Evaluate for Plasmodium parasites.
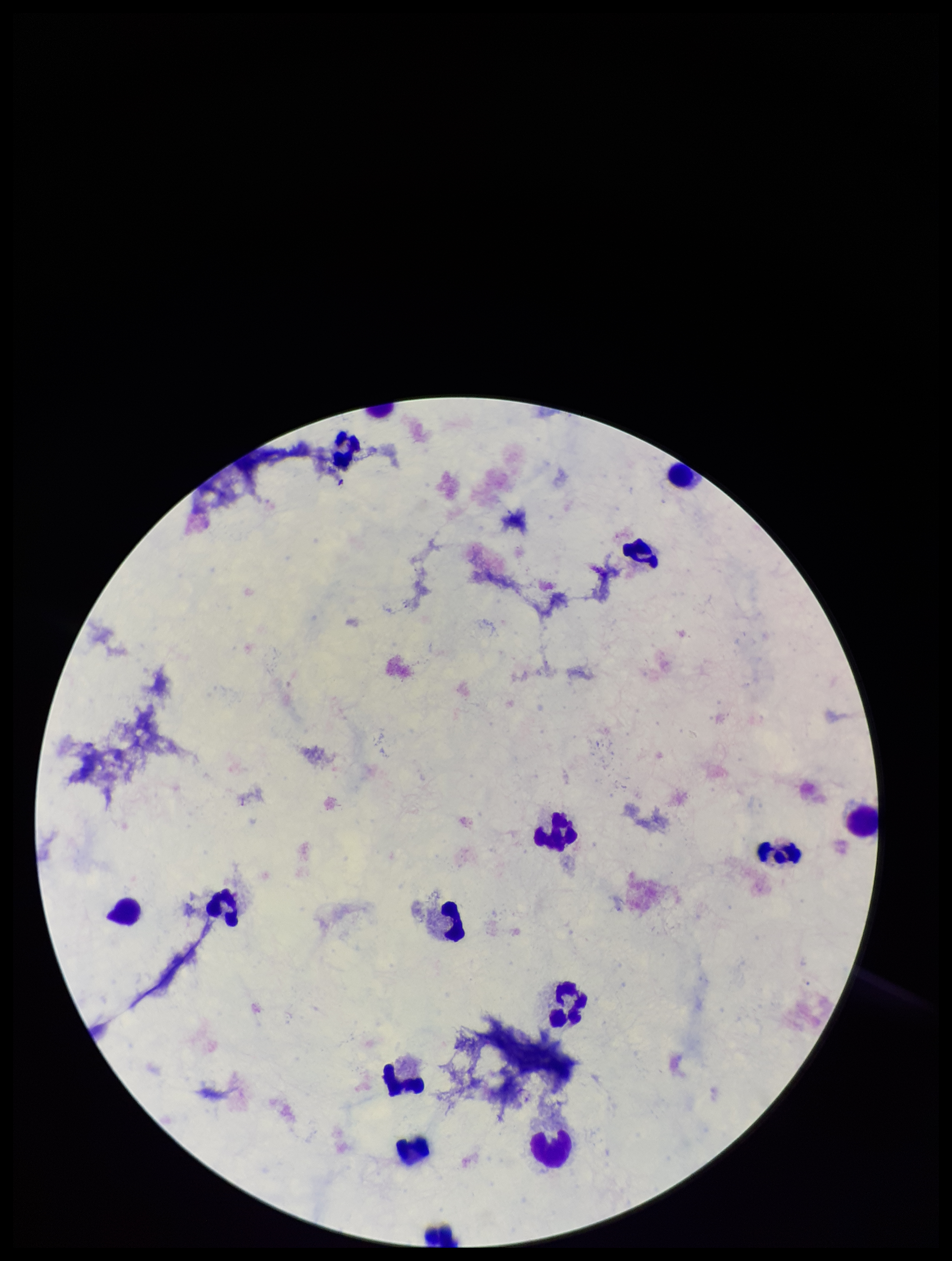

None seen.

Summary:
  - Preparation: thick
  - Parasite count: 0
  - Stain: Giemsa
  - Capture: smartphone photograph through the microscope eyepiece
  - Field of view: one from this slide
  - Patient malaria status: negative
  - Leukocyte count: 14
  - Image size: 952×1261 pixels